Point out cells.
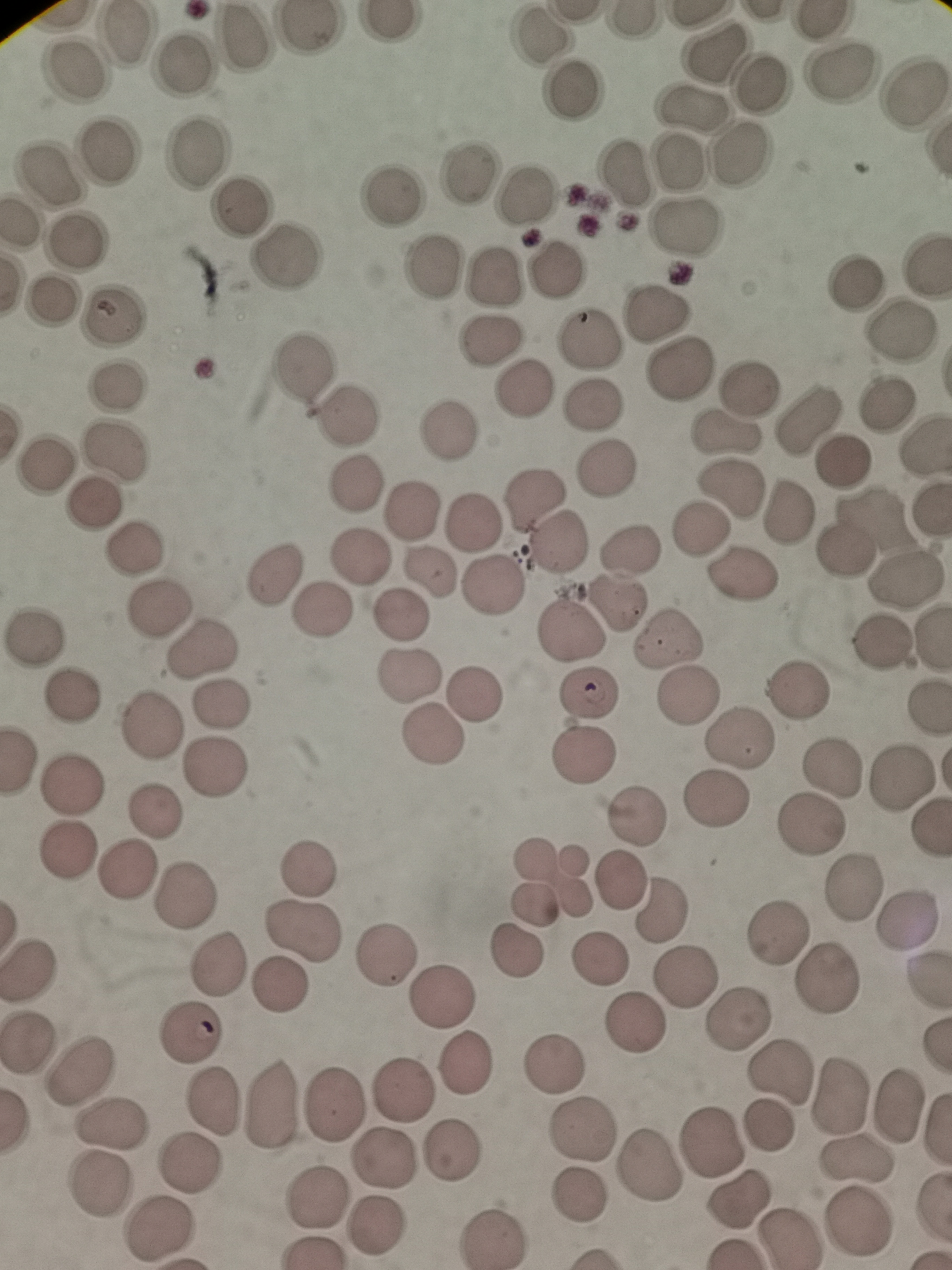

Approximate object centers, in pixels from the top-left corner.
Cells: (x=125, y=31), (x=240, y=38), (x=542, y=38), (x=713, y=49), (x=181, y=68), (x=73, y=70), (x=840, y=74), (x=760, y=81), (x=572, y=89), (x=916, y=95), (x=692, y=104), (x=105, y=150), (x=198, y=151), (x=740, y=153), (x=679, y=158), (x=621, y=171), (x=54, y=173), (x=471, y=175), (x=393, y=195), (x=522, y=196), (x=239, y=209), (x=682, y=224), (x=77, y=238), (x=282, y=258), (x=431, y=268), (x=556, y=269), (x=493, y=276), (x=857, y=287), (x=51, y=299), (x=116, y=315), (x=656, y=315), (x=903, y=333), (x=590, y=341), (x=490, y=344), (x=304, y=366), (x=675, y=369), (x=119, y=383), (x=525, y=385), (x=589, y=406), (x=887, y=409), (x=349, y=414), (x=809, y=421), (x=449, y=431), (x=728, y=436), (x=116, y=447), (x=843, y=460), (x=49, y=462), (x=606, y=469), (x=732, y=483), (x=353, y=485), (x=534, y=496), (x=96, y=504), (x=414, y=510), (x=789, y=513), (x=472, y=524), (x=697, y=526), (x=555, y=545), (x=135, y=549), (x=637, y=549), (x=843, y=551), (x=359, y=558), (x=277, y=572), (x=434, y=575), (x=742, y=576), (x=905, y=581), (x=489, y=586), (x=621, y=603), (x=159, y=607), (x=320, y=611), (x=400, y=617), (x=573, y=633), (x=35, y=634), (x=883, y=641), (x=666, y=643), (x=199, y=654), (x=410, y=676), (x=797, y=685), (x=592, y=688), (x=70, y=694), (x=480, y=696), (x=688, y=696), (x=220, y=705), (x=149, y=724), (x=435, y=735), (x=739, y=739), (x=585, y=755), (x=216, y=764), (x=834, y=765), (x=901, y=779), (x=72, y=781), (x=716, y=798), (x=154, y=814), (x=641, y=817), (x=813, y=823), (x=70, y=846), (x=305, y=867), (x=126, y=873), (x=619, y=881), (x=550, y=884), (x=857, y=887), (x=184, y=895), (x=662, y=911), (x=776, y=929), (x=300, y=933), (x=514, y=949), (x=385, y=951), (x=28, y=964), (x=599, y=965), (x=215, y=967), (x=683, y=976), (x=827, y=979), (x=278, y=984), (x=443, y=998), (x=740, y=1015), (x=190, y=1034), (x=26, y=1039), (x=555, y=1061), (x=470, y=1065), (x=783, y=1068), (x=85, y=1069), (x=405, y=1084), (x=840, y=1091), (x=336, y=1100), (x=216, y=1101), (x=271, y=1101), (x=896, y=1102), (x=767, y=1124), (x=110, y=1127), (x=580, y=1131), (x=709, y=1137), (x=453, y=1150), (x=387, y=1158), (x=857, y=1159), (x=653, y=1164), (x=189, y=1165), (x=97, y=1186), (x=315, y=1195), (x=577, y=1195), (x=742, y=1200), (x=860, y=1221), (x=376, y=1225), (x=158, y=1232), (x=493, y=1237).

capture = smartphone through the microscope eyepiece
image size = 952×1270 pixels
preparation = thin blood smear
field of view = single
stain = Giemsa